Comment on the morphology of the erythrocytes.
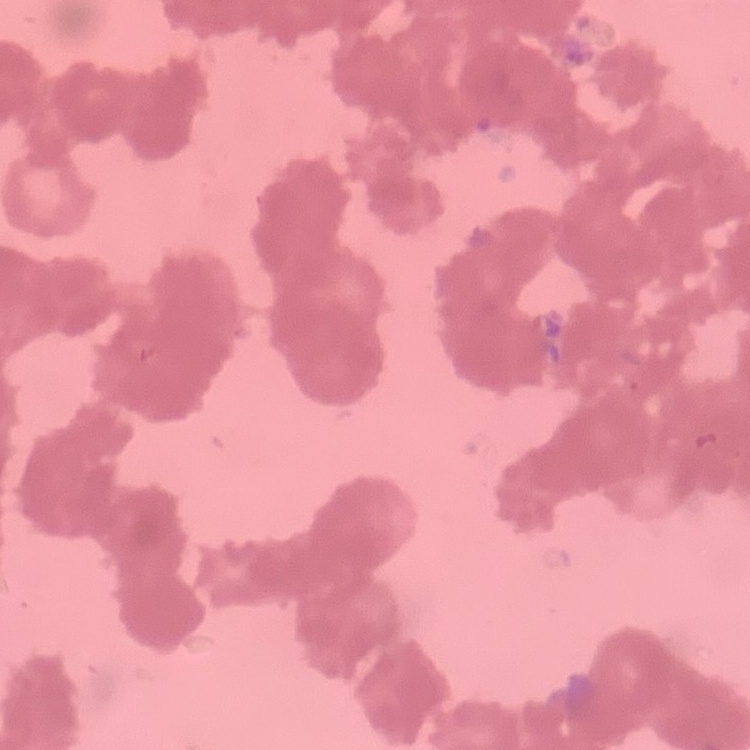
Rouleaux formation.

Field's or Giemsa stain. One tile cut from a larger photomicrograph. Thin blood smear.